Report the malaria status of this cell.
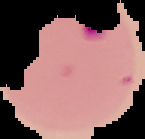

Parasitized.

image_type: segmented cell region on a black background
preparation: thin blood smear
image_size: 145×139 pixels